Name the cell type shown.
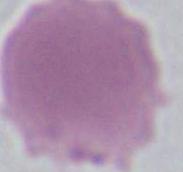

An erythrocyte.

Summary:
  - Modality: micrograph
  - Magnification: 1000x